Give the location of every white blood cell.
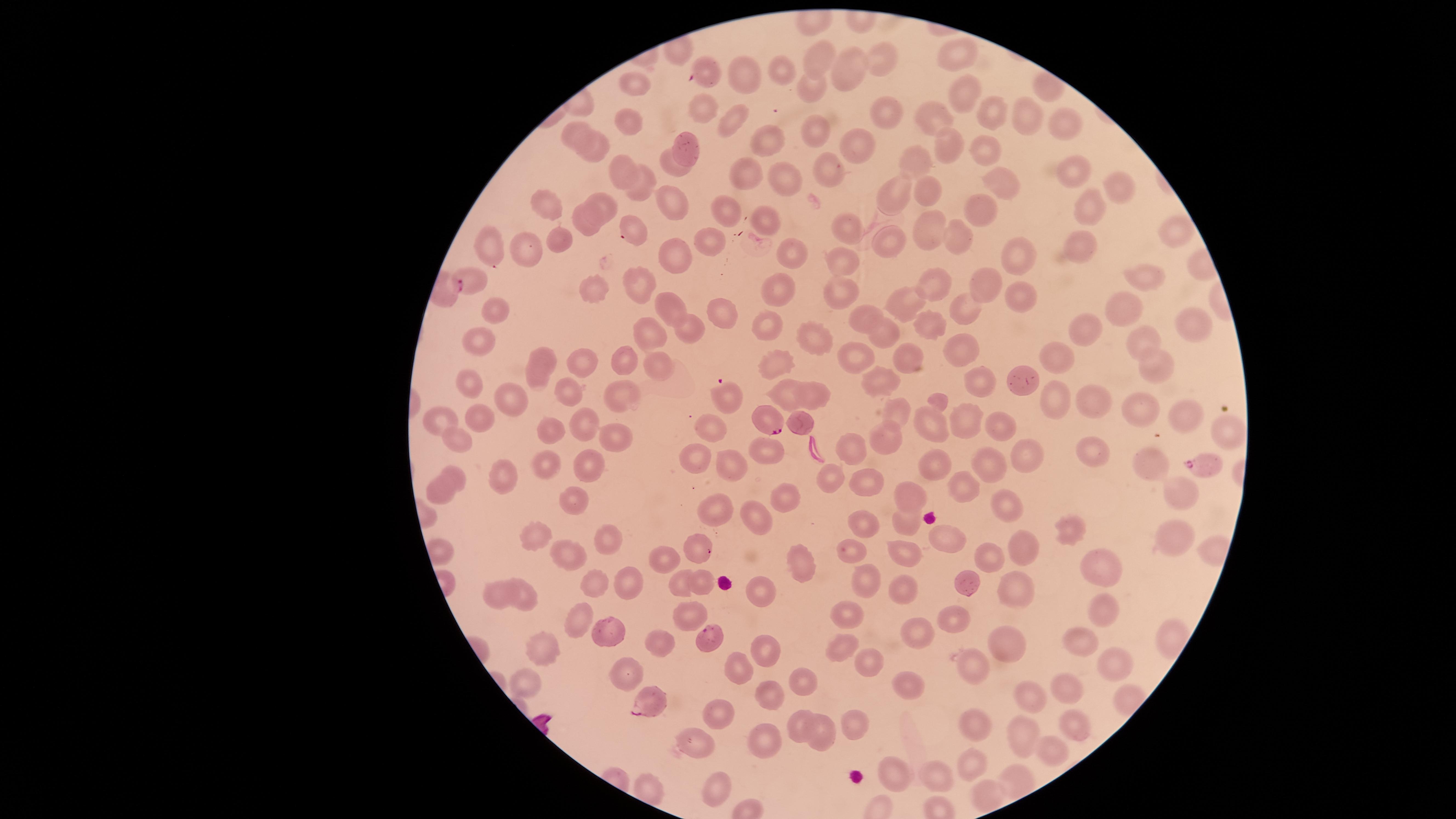
No white blood cells identified.

capture = smartphone photograph through the microscope eyepiece
stain = Giemsa
parasitized red blood cells = approximate marker points, in pixels from the top-left corner: (x=446, y=286), (x=766, y=421), (x=1203, y=464), (x=709, y=638), (x=646, y=701)
uninfected red blood cells = approximate marker points, in pixels from the top-left corner: (x=957, y=53), (x=819, y=55), (x=876, y=60), (x=707, y=65), (x=852, y=66), (x=734, y=69), (x=780, y=71), (x=810, y=85), (x=636, y=86), (x=1047, y=87), (x=959, y=93), (x=702, y=109), (x=884, y=109), (x=989, y=113), (x=931, y=118), (x=1029, y=118), (x=629, y=119), (x=726, y=119), (x=1060, y=122), (x=817, y=129), (x=577, y=130), (x=767, y=136), (x=857, y=142), (x=686, y=144), (x=949, y=146), (x=979, y=147), (x=594, y=152), (x=913, y=159), (x=673, y=161), (x=621, y=168), (x=826, y=169), (x=1076, y=169), (x=1002, y=175), (x=748, y=177), (x=786, y=178), (x=640, y=183), (x=1119, y=186), (x=896, y=190), (x=931, y=191), (x=675, y=199), (x=551, y=202), (x=1090, y=206), (x=606, y=207), (x=727, y=209), (x=983, y=210), (x=586, y=220), (x=765, y=220), (x=631, y=221), (x=927, y=226), (x=844, y=229), (x=1178, y=231), (x=961, y=234), (x=557, y=238), (x=706, y=240), (x=887, y=241), (x=490, y=244), (x=1083, y=245), (x=523, y=249), (x=785, y=252), (x=1010, y=254), (x=677, y=256), (x=845, y=267), (x=477, y=278), (x=1151, y=279), (x=640, y=281), (x=978, y=281), (x=927, y=286), (x=589, y=288), (x=782, y=293), (x=1014, y=295), (x=841, y=296), (x=667, y=302), (x=971, y=305), (x=914, y=307), (x=1123, y=308), (x=499, y=309), (x=721, y=315), (x=769, y=318), (x=869, y=322), (x=1193, y=323), (x=924, y=326), (x=686, y=329), (x=1090, y=331), (x=652, y=332), (x=884, y=335), (x=816, y=340), (x=1143, y=342), (x=481, y=343), (x=955, y=351), (x=547, y=353), (x=1056, y=355), (x=915, y=356), (x=620, y=359), (x=858, y=360), (x=582, y=363), (x=656, y=364), (x=781, y=364), (x=1159, y=368), (x=535, y=372), (x=980, y=378), (x=1022, y=380), (x=880, y=382), (x=477, y=388), (x=789, y=390), (x=564, y=392), (x=814, y=393), (x=728, y=396), (x=621, y=397), (x=521, y=399), (x=1056, y=400), (x=903, y=409), (x=1092, y=409), (x=1138, y=410), (x=1192, y=415), (x=585, y=418), (x=442, y=419), (x=963, y=421), (x=485, y=422), (x=798, y=423), (x=1000, y=425), (x=932, y=426), (x=708, y=429), (x=1230, y=429), (x=555, y=431), (x=888, y=434), (x=453, y=438), (x=613, y=439), (x=852, y=446), (x=760, y=448), (x=1092, y=452), (x=1031, y=454), (x=697, y=456), (x=989, y=457), (x=937, y=461), (x=1155, y=461), (x=585, y=463), (x=541, y=464), (x=737, y=464), (x=500, y=470), (x=826, y=475), (x=456, y=476), (x=868, y=481), (x=968, y=484), (x=436, y=488), (x=1181, y=492), (x=910, y=494), (x=571, y=495), (x=784, y=498), (x=721, y=508), (x=1008, y=509), (x=749, y=516), (x=906, y=518), (x=863, y=526), (x=540, y=532), (x=1073, y=534), (x=944, y=535), (x=610, y=539), (x=1177, y=540), (x=1028, y=547), (x=849, y=548), (x=699, y=549), (x=571, y=554), (x=906, y=555), (x=985, y=559), (x=668, y=562), (x=807, y=562), (x=1101, y=569), (x=868, y=578), (x=700, y=581), (x=626, y=583), (x=684, y=583), (x=593, y=584), (x=906, y=586), (x=1012, y=586), (x=973, y=588), (x=762, y=592), (x=520, y=593), (x=494, y=595), (x=1103, y=612), (x=847, y=613), (x=691, y=615), (x=582, y=619), (x=954, y=620), (x=614, y=631), (x=914, y=631), (x=659, y=639), (x=1079, y=639), (x=1004, y=644), (x=838, y=646), (x=545, y=651), (x=765, y=652), (x=1106, y=656), (x=865, y=661), (x=967, y=664), (x=622, y=665), (x=744, y=670), (x=531, y=683), (x=804, y=684), (x=1069, y=690), (x=906, y=692), (x=1034, y=693), (x=774, y=694), (x=715, y=716), (x=1071, y=719), (x=854, y=721), (x=799, y=724), (x=973, y=725), (x=819, y=730), (x=1021, y=737), (x=770, y=738), (x=695, y=744), (x=1050, y=746), (x=971, y=764), (x=893, y=776), (x=940, y=778), (x=1015, y=782), (x=721, y=784), (x=987, y=797)
visible region = circular
species = Plasmodium falciparum
presence = malaria parasites detected
image size = 1456×819 pixels
preparation = thin blood smear
field of view = single